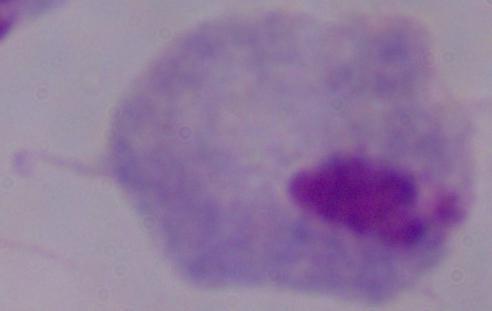
Summary:
  - Modality: photomicrograph
  - Identification: trichomonad
  - Magnification: 1000x